Name the parasite shown.
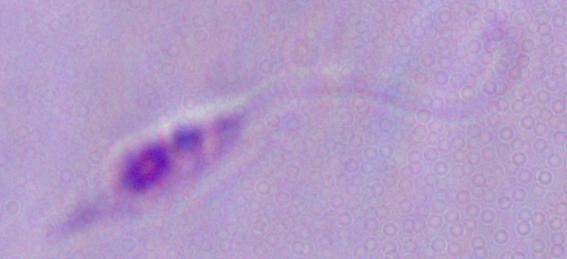

Leishmania.

Captured at 1000x magnification. Micrograph.